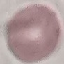 Malaria status: uninfected. Thin blood smear. Giemsa stain. Automatically extracted cell patch, resized to 64 × 64 pixels. Acquired by smartphone through the microscope eyepiece.